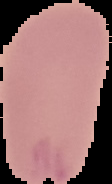

image_type: segmented cell region with the area outside set to black
image_size: 112×184 pixels
preparation: thin blood smear
result: negative for Plasmodium parasites